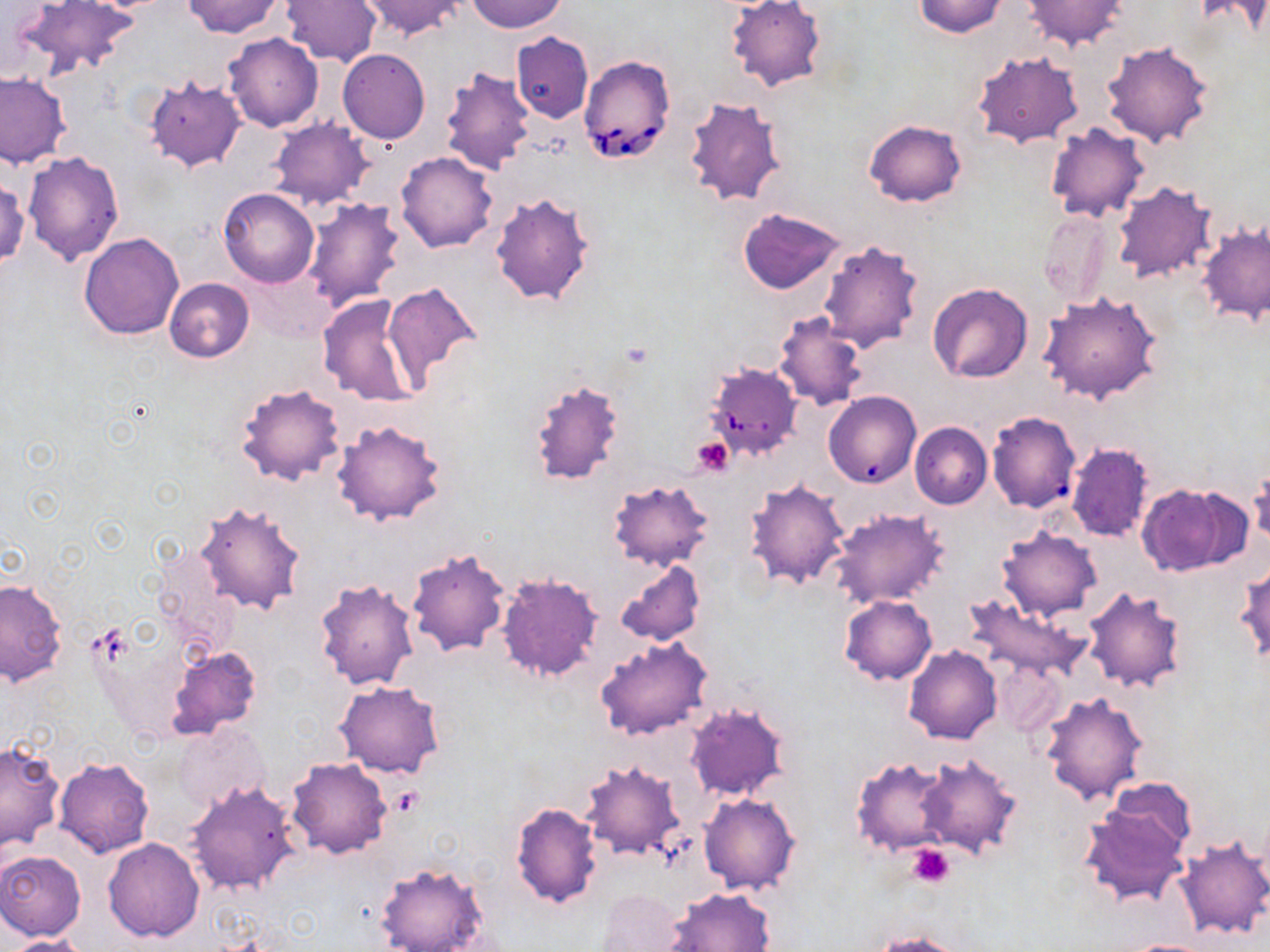
{
  "babesia_divergens_infected_red_blood_cell_locations": "approximate bounding boxes as named x1/y1/x2/y2 corners in pixels: (x1=578, y1=54, x2=675, y2=164), (x1=704, y1=363, x2=804, y2=461)",
  "slide_level_diagnosis": "Babesia divergens",
  "platelet_locations": "approximate bounding boxes as named x1/y1/x2/y2 corners in pixels: (x1=691, y1=437, x2=734, y2=476), (x1=392, y1=786, x2=422, y2=814), (x1=906, y1=844, x2=956, y2=888)",
  "magnification": "1000x",
  "field_of_view": "single",
  "modality": "light microscopy",
  "image_size": "1270×952 pixels",
  "preparation": "thin blood smear",
  "uninfected_red_blood_cell_locations": "approximate bounding boxes as named x1/y1/x2/y2 corners in pixels: (x1=183, y1=0, x2=286, y2=38), (x1=280, y1=0, x2=382, y2=66), (x1=358, y1=0, x2=464, y2=40), (x1=465, y1=0, x2=567, y2=33), (x1=724, y1=0, x2=827, y2=93), (x1=913, y1=0, x2=1008, y2=37), (x1=1024, y1=0, x2=1128, y2=51), (x1=1193, y1=0, x2=1270, y2=37), (x1=16, y1=1, x2=139, y2=76), (x1=511, y1=32, x2=593, y2=123), (x1=223, y1=33, x2=322, y2=132), (x1=1102, y1=41, x2=1214, y2=148), (x1=338, y1=49, x2=430, y2=144), (x1=972, y1=51, x2=1082, y2=148), (x1=437, y1=64, x2=535, y2=174), (x1=0, y1=73, x2=72, y2=168), (x1=145, y1=77, x2=246, y2=173), (x1=683, y1=94, x2=791, y2=208), (x1=269, y1=117, x2=374, y2=210), (x1=864, y1=119, x2=966, y2=206), (x1=1045, y1=124, x2=1149, y2=223), (x1=22, y1=152, x2=124, y2=266), (x1=396, y1=152, x2=498, y2=252), (x1=0, y1=177, x2=29, y2=269), (x1=1112, y1=181, x2=1217, y2=285), (x1=219, y1=188, x2=320, y2=288), (x1=489, y1=189, x2=598, y2=307), (x1=303, y1=198, x2=408, y2=312), (x1=737, y1=207, x2=846, y2=294), (x1=1040, y1=210, x2=1112, y2=309), (x1=1197, y1=219, x2=1270, y2=327), (x1=78, y1=232, x2=184, y2=340), (x1=817, y1=238, x2=924, y2=354), (x1=163, y1=278, x2=253, y2=363), (x1=383, y1=282, x2=484, y2=385), (x1=926, y1=282, x2=1033, y2=383), (x1=1038, y1=291, x2=1164, y2=404), (x1=317, y1=294, x2=423, y2=408), (x1=773, y1=310, x2=868, y2=412), (x1=529, y1=377, x2=624, y2=487), (x1=234, y1=382, x2=348, y2=487), (x1=824, y1=388, x2=917, y2=489), (x1=986, y1=413, x2=1076, y2=518), (x1=332, y1=420, x2=446, y2=525), (x1=910, y1=422, x2=991, y2=509), (x1=1066, y1=442, x2=1153, y2=542), (x1=1248, y1=464, x2=1270, y2=550), (x1=607, y1=478, x2=714, y2=573), (x1=745, y1=478, x2=850, y2=588), (x1=1136, y1=482, x2=1248, y2=576), (x1=195, y1=501, x2=307, y2=617), (x1=827, y1=508, x2=949, y2=610), (x1=996, y1=527, x2=1102, y2=621), (x1=405, y1=547, x2=510, y2=658), (x1=614, y1=561, x2=706, y2=647), (x1=1235, y1=563, x2=1270, y2=662), (x1=495, y1=572, x2=603, y2=684), (x1=0, y1=576, x2=67, y2=687), (x1=315, y1=579, x2=420, y2=690), (x1=1082, y1=587, x2=1190, y2=694), (x1=838, y1=595, x2=936, y2=684), (x1=964, y1=595, x2=1088, y2=681), (x1=595, y1=637, x2=714, y2=740), (x1=168, y1=646, x2=261, y2=740), (x1=904, y1=646, x2=1001, y2=744), (x1=994, y1=658, x2=1065, y2=736), (x1=334, y1=679, x2=445, y2=778), (x1=1040, y1=692, x2=1150, y2=805), (x1=683, y1=701, x2=791, y2=802), (x1=175, y1=722, x2=271, y2=814), (x1=0, y1=742, x2=66, y2=855), (x1=916, y1=752, x2=1022, y2=857), (x1=850, y1=755, x2=955, y2=856), (x1=53, y1=757, x2=154, y2=857), (x1=287, y1=757, x2=392, y2=859), (x1=579, y1=758, x2=688, y2=863), (x1=1102, y1=776, x2=1198, y2=860), (x1=185, y1=778, x2=301, y2=895), (x1=698, y1=793, x2=801, y2=896), (x1=510, y1=802, x2=602, y2=908), (x1=1078, y1=805, x2=1191, y2=906), (x1=1174, y1=837, x2=1270, y2=940), (x1=103, y1=838, x2=204, y2=943), (x1=0, y1=850, x2=86, y2=941), (x1=375, y1=862, x2=489, y2=952), (x1=664, y1=887, x2=775, y2=951), (x1=598, y1=888, x2=691, y2=952), (x1=868, y1=932, x2=968, y2=952), (x1=5, y1=934, x2=89, y2=952), (x1=1120, y1=938, x2=1221, y2=951)",
  "stain": "May-Grünwald-Giemsa"
}